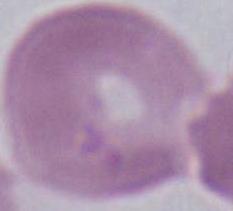
modality: micrograph
magnification: 1000x
identification: red blood cell